Report the malaria status of this cell.
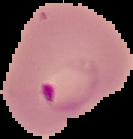
It is parasitized.

Cell region segmented out of the field of view; the surrounding area is masked to black. From a thin blood film. Image is 133×139 pixels.